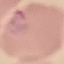
result = malaria parasites identified
capture = smartphone camera at the microscope eyepiece
preparation = thin blood film
image type = automatically extracted cell patch, resized to 64 × 64 pixels
stain = Giemsa